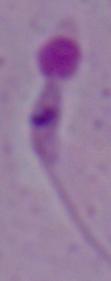
identification = Leishmania
magnification = 1000x
modality = micrograph